Give the preparation type.
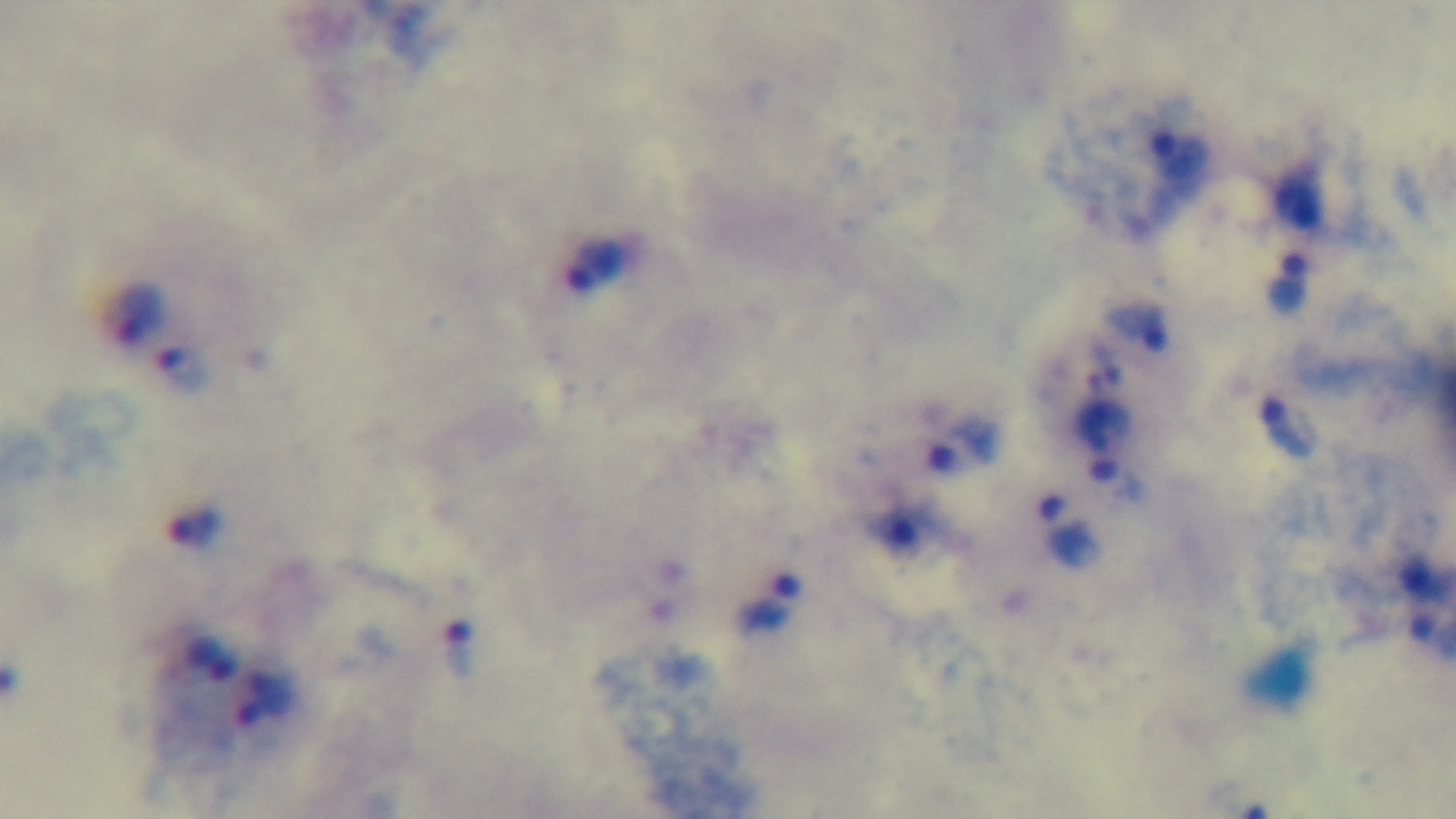
It is a thick blood film.

Light microscopy. 100x oil-immersion objective. Captured with a mounted 4K digital camera. One field from the slide. Malaria status: infected. Giemsa stain.